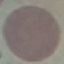

Malaria status: uninfected. Thin blood film. Cell patch, automatically extracted from a larger field of view and resized to 64 × 64 pixels. Giemsa-stained preparation. Photographed with a smartphone camera at the microscope eyepiece.